Report the malaria status.
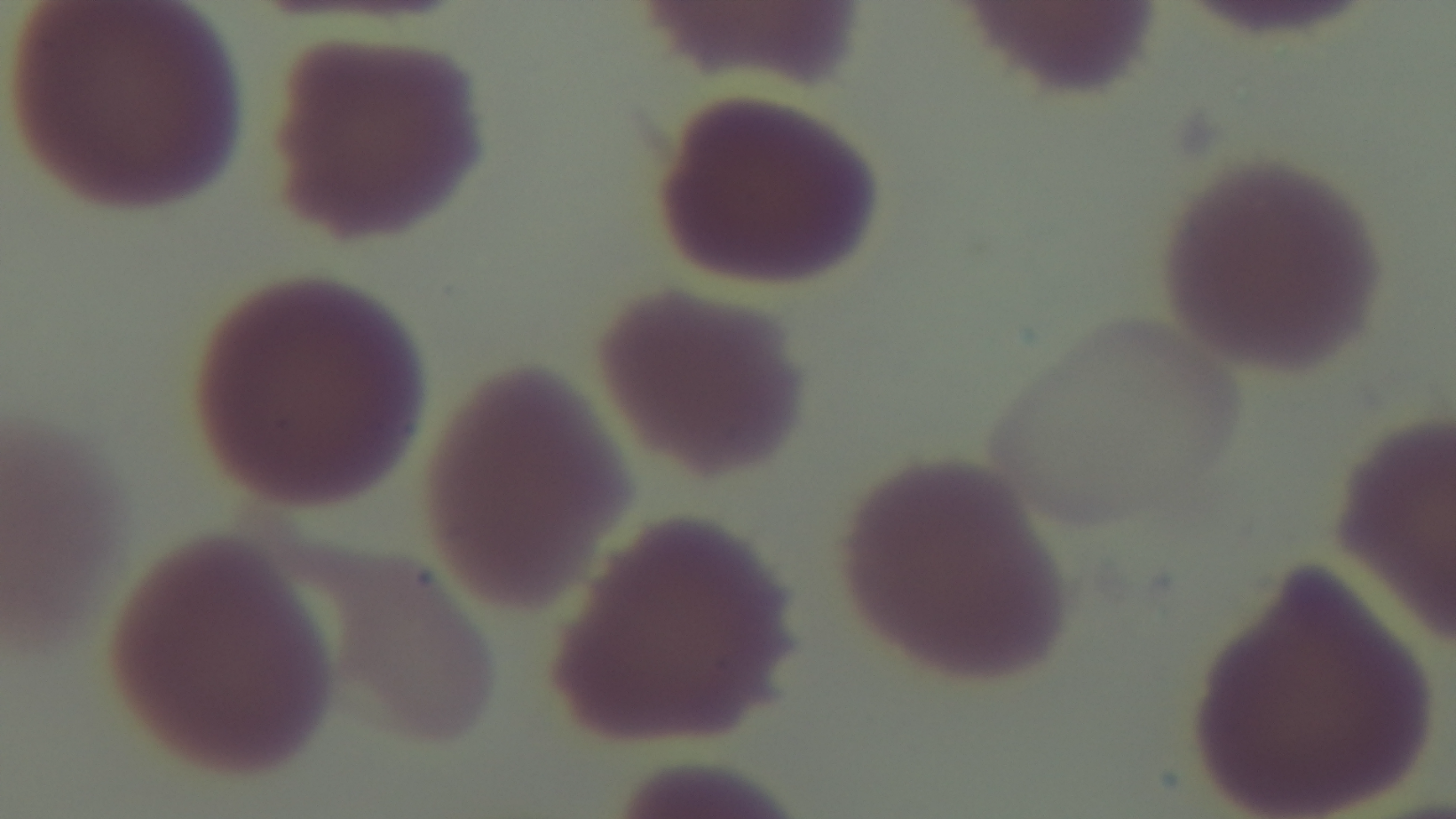

Negative.

Summary:
  - Modality: light microscopy
  - Preparation: thin blood film
  - Field of view: one from the slide
  - Stain: Giemsa
  - Capture: mounted 4K digital camera
  - Objective: 100x oil immersion